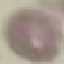

Summary:
  - Result: no malaria parasites seen
  - Stain: Giemsa
  - Capture: smartphone camera at the microscope eyepiece
  - Image type: automatically extracted cell patch, resized to 64 × 64 pixels
  - Preparation: thin blood film